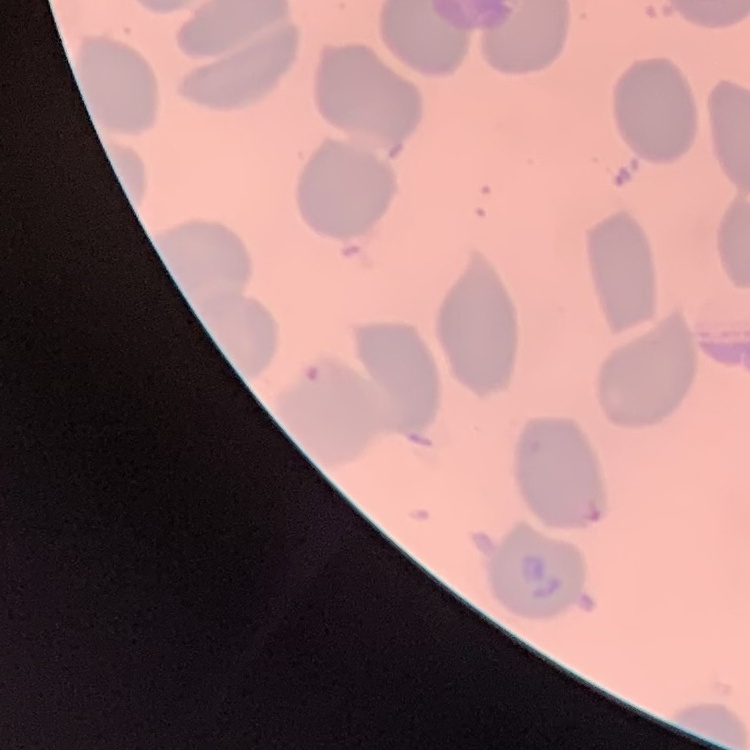
{
  "erythrocyte_morphology": "no rouleaux formation",
  "image_type": "square crop of a larger photomicrograph",
  "stain": "Field's or Giemsa",
  "preparation": "thin blood film"
}